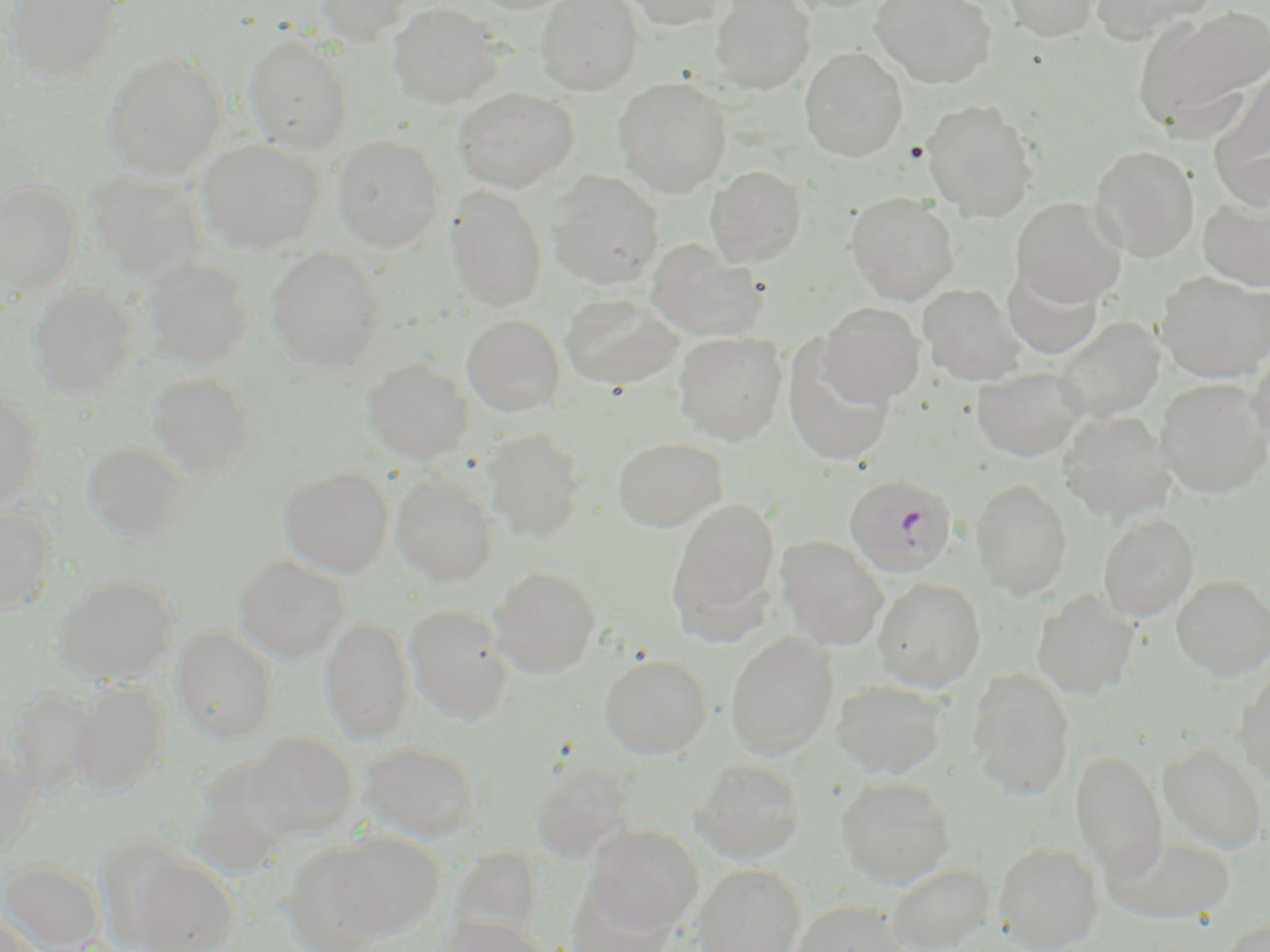
Summary:
  - Coordinate format: approximate bounding boxes as named x1/y1/x2/y2 corners in pixels
  - Plasmodium falciparum-infected red blood cell locations: (x1=846, y1=473, x2=957, y2=577)
  - Uninfected red blood cell locations: (x1=6, y1=0, x2=126, y2=84), (x1=314, y1=0, x2=418, y2=46), (x1=467, y1=0, x2=582, y2=14), (x1=536, y1=0, x2=644, y2=95), (x1=618, y1=0, x2=732, y2=30), (x1=782, y1=0, x2=891, y2=14), (x1=871, y1=0, x2=997, y2=88), (x1=1000, y1=0, x2=1105, y2=41), (x1=1089, y1=0, x2=1216, y2=43), (x1=712, y1=1, x2=815, y2=95), (x1=388, y1=2, x2=502, y2=107), (x1=1132, y1=6, x2=1270, y2=134), (x1=244, y1=34, x2=352, y2=153), (x1=800, y1=47, x2=907, y2=162), (x1=102, y1=50, x2=227, y2=179), (x1=1210, y1=67, x2=1270, y2=198), (x1=613, y1=77, x2=732, y2=195), (x1=454, y1=88, x2=578, y2=192), (x1=920, y1=98, x2=1040, y2=221), (x1=332, y1=135, x2=445, y2=252), (x1=198, y1=139, x2=324, y2=253), (x1=1090, y1=144, x2=1200, y2=261), (x1=706, y1=165, x2=807, y2=267), (x1=87, y1=171, x2=206, y2=281), (x1=548, y1=171, x2=664, y2=289), (x1=0, y1=180, x2=81, y2=294), (x1=445, y1=185, x2=548, y2=313), (x1=845, y1=192, x2=960, y2=304), (x1=1198, y1=193, x2=1270, y2=292), (x1=1011, y1=198, x2=1127, y2=305), (x1=646, y1=240, x2=768, y2=341), (x1=266, y1=247, x2=385, y2=371), (x1=143, y1=258, x2=253, y2=368), (x1=1003, y1=262, x2=1105, y2=359), (x1=1156, y1=271, x2=1270, y2=382), (x1=918, y1=284, x2=1024, y2=385), (x1=29, y1=285, x2=136, y2=398), (x1=560, y1=293, x2=684, y2=390), (x1=818, y1=303, x2=925, y2=404), (x1=462, y1=315, x2=565, y2=416), (x1=1051, y1=317, x2=1165, y2=422), (x1=674, y1=331, x2=787, y2=445), (x1=783, y1=340, x2=895, y2=468), (x1=1247, y1=342, x2=1270, y2=448), (x1=362, y1=359, x2=473, y2=463), (x1=973, y1=366, x2=1087, y2=461), (x1=147, y1=372, x2=253, y2=481), (x1=1154, y1=378, x2=1270, y2=498), (x1=0, y1=386, x2=43, y2=508), (x1=1057, y1=411, x2=1177, y2=522), (x1=482, y1=428, x2=586, y2=543), (x1=613, y1=437, x2=726, y2=532), (x1=83, y1=443, x2=188, y2=542), (x1=278, y1=467, x2=394, y2=577), (x1=391, y1=475, x2=497, y2=586), (x1=971, y1=478, x2=1073, y2=600), (x1=667, y1=499, x2=781, y2=635), (x1=0, y1=505, x2=57, y2=614), (x1=1098, y1=515, x2=1197, y2=621), (x1=776, y1=536, x2=888, y2=648), (x1=233, y1=556, x2=350, y2=664), (x1=490, y1=566, x2=602, y2=677), (x1=1171, y1=574, x2=1270, y2=681), (x1=52, y1=575, x2=179, y2=684), (x1=873, y1=578, x2=985, y2=691), (x1=1033, y1=590, x2=1139, y2=700), (x1=404, y1=605, x2=513, y2=725), (x1=320, y1=617, x2=414, y2=744), (x1=171, y1=627, x2=279, y2=743), (x1=725, y1=632, x2=839, y2=759), (x1=599, y1=655, x2=711, y2=759), (x1=1234, y1=670, x2=1270, y2=786), (x1=966, y1=672, x2=1074, y2=801), (x1=70, y1=679, x2=169, y2=795), (x1=832, y1=679, x2=947, y2=778), (x1=6, y1=688, x2=96, y2=799), (x1=244, y1=731, x2=359, y2=838), (x1=359, y1=741, x2=480, y2=843), (x1=1158, y1=742, x2=1268, y2=853), (x1=1071, y1=750, x2=1167, y2=878), (x1=0, y1=753, x2=37, y2=859), (x1=186, y1=759, x2=298, y2=877), (x1=691, y1=760, x2=804, y2=863), (x1=529, y1=763, x2=638, y2=862), (x1=837, y1=777, x2=956, y2=887), (x1=584, y1=825, x2=702, y2=933), (x1=328, y1=832, x2=444, y2=937), (x1=1102, y1=834, x2=1236, y2=924), (x1=994, y1=842, x2=1102, y2=951), (x1=282, y1=843, x2=393, y2=952), (x1=451, y1=846, x2=543, y2=940), (x1=131, y1=855, x2=238, y2=952), (x1=0, y1=858, x2=106, y2=952), (x1=695, y1=863, x2=805, y2=952), (x1=888, y1=863, x2=994, y2=952), (x1=567, y1=881, x2=674, y2=952), (x1=792, y1=900, x2=909, y2=952), (x1=0, y1=908, x2=41, y2=952), (x1=436, y1=915, x2=548, y2=952), (x1=1220, y1=917, x2=1269, y2=952)
  - Slide-level diagnosis: Plasmodium falciparum
  - Field of view: single
  - Image size: 1270×952 pixels
  - Preparation: thin blood film
  - Magnification: 1000x
  - Modality: light microscopy
  - Stain: May-Grünwald-Giemsa